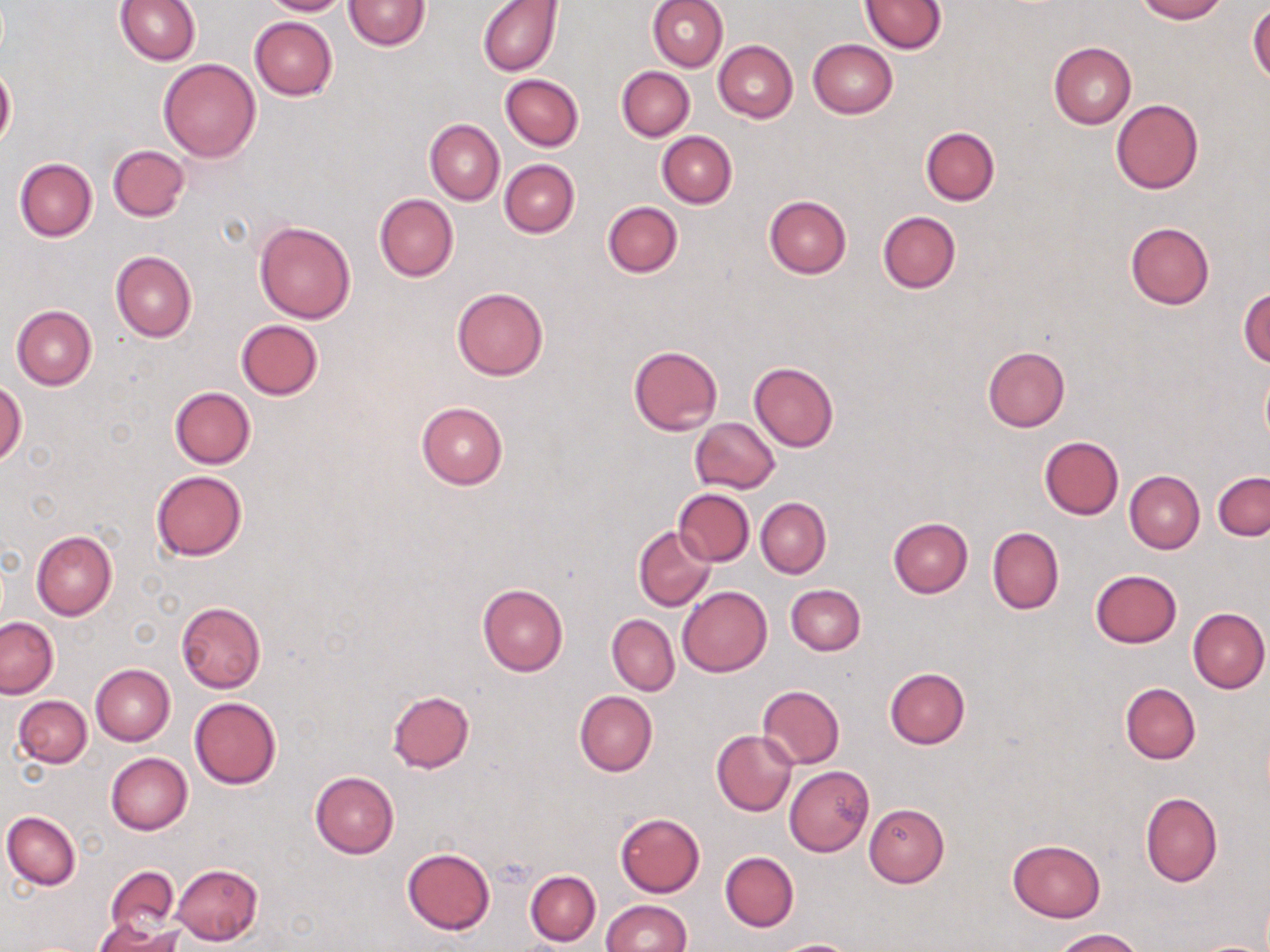
Approximate bounding boxes as named x1/y1/x2/y2 corners in pixels. Platelet locations: (x1=493, y1=856, x2=534, y2=887). Uninfected red blood cell locations: (x1=115, y1=0, x2=202, y2=65), (x1=261, y1=0, x2=350, y2=16), (x1=342, y1=0, x2=431, y2=50), (x1=478, y1=0, x2=562, y2=76), (x1=646, y1=0, x2=728, y2=71), (x1=1135, y1=0, x2=1226, y2=22), (x1=860, y1=1, x2=945, y2=54), (x1=1248, y1=4, x2=1270, y2=85), (x1=249, y1=17, x2=337, y2=100), (x1=807, y1=39, x2=898, y2=118), (x1=713, y1=41, x2=798, y2=123), (x1=1048, y1=42, x2=1136, y2=128), (x1=158, y1=58, x2=261, y2=163), (x1=0, y1=61, x2=16, y2=153), (x1=617, y1=66, x2=694, y2=141), (x1=500, y1=74, x2=583, y2=151), (x1=1111, y1=99, x2=1203, y2=194), (x1=425, y1=119, x2=504, y2=206), (x1=920, y1=126, x2=1000, y2=206), (x1=657, y1=132, x2=737, y2=208), (x1=106, y1=145, x2=190, y2=222), (x1=14, y1=158, x2=98, y2=241), (x1=499, y1=159, x2=579, y2=238), (x1=374, y1=194, x2=458, y2=281), (x1=764, y1=195, x2=852, y2=278), (x1=603, y1=202, x2=683, y2=279), (x1=878, y1=211, x2=960, y2=293), (x1=254, y1=221, x2=356, y2=324), (x1=1125, y1=222, x2=1215, y2=309), (x1=110, y1=250, x2=197, y2=342), (x1=451, y1=287, x2=549, y2=382), (x1=1239, y1=288, x2=1270, y2=367), (x1=11, y1=305, x2=97, y2=389), (x1=236, y1=320, x2=323, y2=399), (x1=628, y1=344, x2=723, y2=436), (x1=983, y1=346, x2=1070, y2=432), (x1=749, y1=363, x2=839, y2=452), (x1=1260, y1=370, x2=1270, y2=447), (x1=1, y1=379, x2=26, y2=466), (x1=169, y1=385, x2=256, y2=468), (x1=416, y1=401, x2=508, y2=489), (x1=690, y1=417, x2=780, y2=493), (x1=1039, y1=436, x2=1123, y2=519), (x1=150, y1=468, x2=248, y2=562), (x1=1124, y1=470, x2=1204, y2=554), (x1=1213, y1=472, x2=1270, y2=540), (x1=674, y1=489, x2=754, y2=566), (x1=756, y1=497, x2=830, y2=578), (x1=888, y1=517, x2=973, y2=597), (x1=634, y1=525, x2=716, y2=612), (x1=987, y1=527, x2=1064, y2=614), (x1=31, y1=530, x2=117, y2=619), (x1=1089, y1=569, x2=1183, y2=648), (x1=477, y1=584, x2=569, y2=676), (x1=786, y1=584, x2=865, y2=656), (x1=677, y1=586, x2=772, y2=676), (x1=176, y1=602, x2=266, y2=692), (x1=1187, y1=606, x2=1269, y2=693), (x1=607, y1=615, x2=679, y2=695), (x1=0, y1=616, x2=58, y2=699), (x1=90, y1=663, x2=175, y2=746), (x1=884, y1=667, x2=970, y2=749), (x1=1120, y1=683, x2=1201, y2=764), (x1=757, y1=685, x2=845, y2=768), (x1=387, y1=690, x2=475, y2=772), (x1=574, y1=691, x2=657, y2=777), (x1=13, y1=696, x2=91, y2=768), (x1=189, y1=698, x2=282, y2=789), (x1=711, y1=730, x2=798, y2=817), (x1=104, y1=752, x2=192, y2=836), (x1=783, y1=766, x2=874, y2=856), (x1=309, y1=772, x2=399, y2=858), (x1=1140, y1=792, x2=1221, y2=888), (x1=864, y1=803, x2=949, y2=887), (x1=3, y1=811, x2=81, y2=889), (x1=614, y1=812, x2=706, y2=896), (x1=1007, y1=839, x2=1107, y2=922), (x1=402, y1=847, x2=495, y2=935), (x1=719, y1=851, x2=798, y2=932), (x1=172, y1=863, x2=263, y2=945), (x1=104, y1=866, x2=181, y2=937), (x1=525, y1=869, x2=601, y2=946), (x1=600, y1=901, x2=690, y2=952), (x1=93, y1=920, x2=182, y2=952), (x1=1053, y1=928, x2=1145, y2=951), (x1=773, y1=938, x2=861, y2=952). Slide-level diagnosis: no evidence of blood parasites. Light microscopy. Captured at 1000x magnification. Thin blood smear. Image is 1270×952 pixels. May-Grünwald-Giemsa stain. One field of a larger specimen.